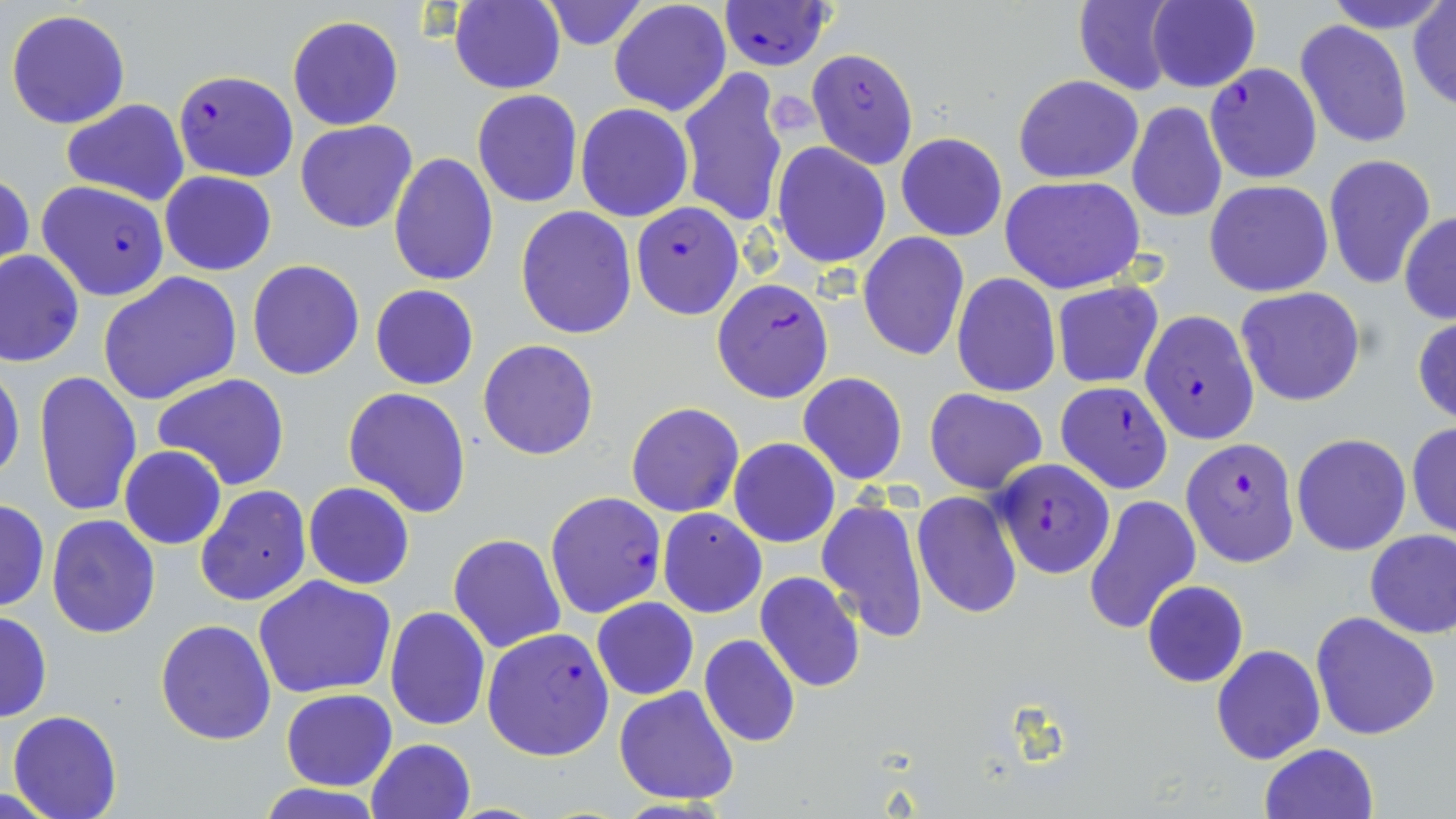
Approximate bounding boxes as named x1/y1/x2/y2 corners in pixels. Uninfected red blood cell locations: (x1=540, y1=0, x2=649, y2=50), (x1=608, y1=0, x2=731, y2=117), (x1=1073, y1=0, x2=1180, y2=96), (x1=1149, y1=0, x2=1260, y2=92), (x1=1324, y1=0, x2=1449, y2=33), (x1=449, y1=1, x2=566, y2=94), (x1=1409, y1=2, x2=1456, y2=111), (x1=5, y1=7, x2=131, y2=130), (x1=286, y1=15, x2=405, y2=131), (x1=1295, y1=19, x2=1413, y2=148), (x1=677, y1=68, x2=791, y2=228), (x1=1013, y1=75, x2=1143, y2=184), (x1=471, y1=90, x2=583, y2=208), (x1=60, y1=99, x2=190, y2=206), (x1=1127, y1=102, x2=1227, y2=224), (x1=575, y1=103, x2=694, y2=221), (x1=296, y1=121, x2=419, y2=233), (x1=896, y1=132, x2=1008, y2=241), (x1=773, y1=143, x2=891, y2=267), (x1=388, y1=153, x2=500, y2=287), (x1=1323, y1=153, x2=1437, y2=291), (x1=1, y1=171, x2=34, y2=278), (x1=160, y1=171, x2=276, y2=275), (x1=1000, y1=175, x2=1145, y2=293), (x1=1205, y1=179, x2=1334, y2=298), (x1=515, y1=207, x2=637, y2=339), (x1=1399, y1=212, x2=1456, y2=323), (x1=857, y1=232, x2=970, y2=361), (x1=1, y1=251, x2=83, y2=367), (x1=246, y1=259, x2=365, y2=380), (x1=99, y1=271, x2=242, y2=405), (x1=951, y1=273, x2=1061, y2=397), (x1=1051, y1=283, x2=1163, y2=387), (x1=369, y1=284, x2=478, y2=389), (x1=1236, y1=287, x2=1366, y2=407), (x1=1414, y1=315, x2=1456, y2=425), (x1=477, y1=339, x2=599, y2=460), (x1=0, y1=362, x2=25, y2=488), (x1=33, y1=371, x2=142, y2=517), (x1=798, y1=372, x2=908, y2=485), (x1=153, y1=374, x2=292, y2=491), (x1=343, y1=387, x2=473, y2=518), (x1=925, y1=388, x2=1048, y2=494), (x1=626, y1=402, x2=744, y2=517), (x1=1407, y1=422, x2=1456, y2=540), (x1=1292, y1=433, x2=1411, y2=557), (x1=729, y1=438, x2=840, y2=548), (x1=118, y1=446, x2=227, y2=550), (x1=303, y1=482, x2=415, y2=589), (x1=194, y1=483, x2=310, y2=607), (x1=913, y1=491, x2=1022, y2=619), (x1=1083, y1=494, x2=1201, y2=634), (x1=816, y1=495, x2=930, y2=642), (x1=0, y1=497, x2=50, y2=613), (x1=658, y1=509, x2=766, y2=617), (x1=45, y1=515, x2=162, y2=638), (x1=1365, y1=528, x2=1456, y2=640), (x1=448, y1=534, x2=566, y2=653), (x1=755, y1=571, x2=866, y2=694), (x1=254, y1=575, x2=399, y2=699), (x1=1142, y1=580, x2=1250, y2=687), (x1=591, y1=597, x2=700, y2=700), (x1=386, y1=606, x2=490, y2=730), (x1=0, y1=610, x2=53, y2=722), (x1=1310, y1=611, x2=1441, y2=741), (x1=154, y1=618, x2=277, y2=745), (x1=700, y1=634, x2=801, y2=747), (x1=1212, y1=645, x2=1324, y2=765), (x1=614, y1=685, x2=741, y2=804), (x1=281, y1=688, x2=397, y2=791), (x1=8, y1=709, x2=123, y2=819), (x1=366, y1=738, x2=475, y2=819), (x1=1259, y1=743, x2=1378, y2=819), (x1=258, y1=782, x2=383, y2=818). Plasmodium falciparum-infected red blood cell locations: (x1=717, y1=1, x2=836, y2=71), (x1=806, y1=48, x2=919, y2=169), (x1=1204, y1=63, x2=1322, y2=183), (x1=172, y1=69, x2=298, y2=181), (x1=37, y1=180, x2=170, y2=301), (x1=631, y1=201, x2=744, y2=320), (x1=711, y1=278, x2=834, y2=403), (x1=1139, y1=311, x2=1260, y2=445), (x1=1055, y1=380, x2=1174, y2=493), (x1=1181, y1=437, x2=1301, y2=567), (x1=991, y1=459, x2=1114, y2=579), (x1=545, y1=492, x2=667, y2=618), (x1=482, y1=626, x2=616, y2=761). Slide-level diagnosis: Plasmodium falciparum. Thin blood film. Captured at 1000x magnification. May-Grünwald-Giemsa stain. Image is 1456×819 pixels. Optical microscopy. One field of a larger specimen.